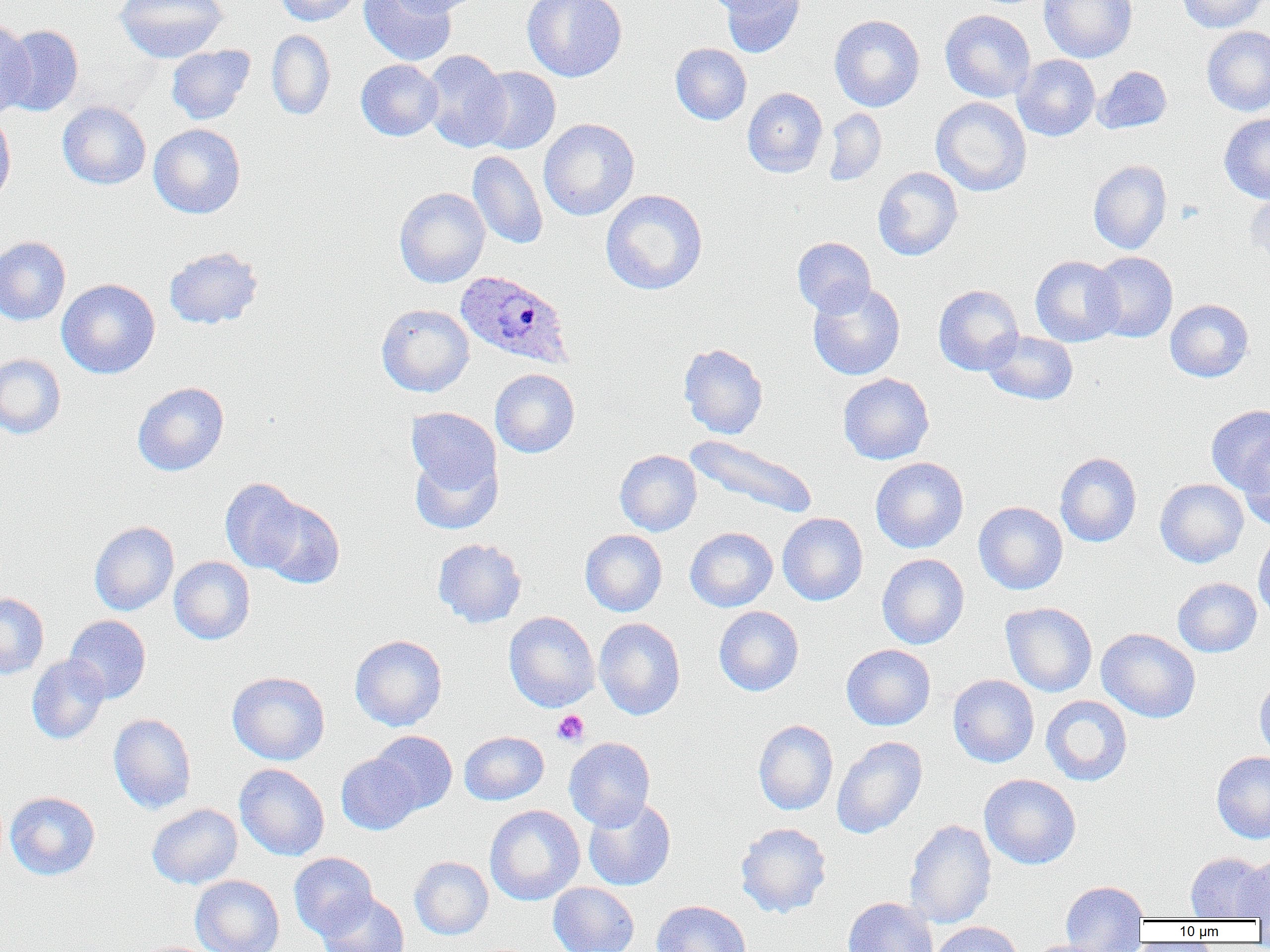

Approximate bounding boxes as [x1, y1, x2, y2] in pixels. Plasmodium ovale-infected red blood cell locations: [455, 269, 574, 369]. Platelet locations: [552, 709, 589, 746]. Uninfected red blood cell locations: [115, 0, 228, 63], [274, 0, 363, 26], [359, 0, 457, 66], [389, 0, 481, 16], [522, 0, 627, 82], [701, 0, 795, 18], [718, 0, 807, 58], [1039, 0, 1137, 63], [1177, 0, 1267, 33], [940, 10, 1036, 102], [829, 14, 925, 112], [0, 17, 35, 119], [1, 24, 83, 117], [1201, 26, 1270, 116], [266, 30, 336, 120], [670, 43, 752, 125], [166, 45, 255, 125], [420, 49, 511, 152], [1013, 55, 1100, 141], [355, 59, 443, 141], [1094, 65, 1172, 134], [473, 67, 560, 154], [742, 87, 828, 178], [931, 97, 1031, 196], [57, 101, 151, 189], [0, 108, 16, 209], [823, 108, 887, 186], [1219, 114, 1270, 203], [538, 118, 639, 221], [149, 123, 246, 218], [467, 150, 548, 249], [1088, 160, 1172, 255], [872, 167, 963, 261], [394, 187, 490, 287], [1246, 187, 1270, 268], [600, 189, 708, 295], [0, 236, 71, 325], [792, 237, 876, 317], [164, 246, 264, 329], [1088, 251, 1178, 342], [1030, 255, 1123, 347], [56, 279, 160, 379], [807, 282, 905, 381], [933, 284, 1024, 375], [1165, 299, 1253, 382], [376, 303, 474, 397], [982, 331, 1079, 405], [678, 343, 768, 439], [0, 353, 66, 439], [490, 368, 580, 457], [838, 373, 934, 464], [132, 382, 229, 476], [1206, 405, 1270, 494], [406, 407, 501, 494], [684, 434, 818, 520], [1238, 438, 1270, 531], [614, 449, 702, 536], [409, 450, 502, 535], [1054, 452, 1142, 547], [870, 457, 969, 553], [220, 477, 306, 573], [1155, 479, 1248, 567], [257, 497, 344, 589], [973, 501, 1068, 594], [777, 513, 867, 605], [89, 521, 179, 615], [685, 527, 777, 612], [580, 530, 667, 616], [1253, 532, 1270, 622], [432, 538, 527, 628], [877, 553, 969, 649], [169, 556, 255, 645], [1172, 577, 1262, 657], [0, 593, 49, 679], [1001, 602, 1097, 696], [714, 606, 804, 696], [504, 611, 600, 712], [64, 615, 151, 704], [594, 618, 685, 720], [1096, 628, 1201, 723], [349, 634, 447, 731], [841, 644, 935, 730], [27, 654, 110, 744], [227, 671, 329, 765], [1254, 673, 1270, 762], [948, 674, 1039, 767], [1041, 695, 1133, 786], [108, 713, 196, 814], [753, 719, 839, 815], [370, 730, 457, 814], [459, 730, 549, 805], [831, 736, 928, 839], [564, 737, 655, 830], [1211, 751, 1270, 843], [336, 753, 422, 835], [235, 764, 329, 861], [979, 774, 1081, 869], [4, 791, 100, 881], [583, 797, 676, 891], [146, 803, 243, 889], [485, 805, 584, 905], [904, 819, 996, 929], [735, 822, 832, 918], [289, 852, 377, 939], [1185, 852, 1268, 920], [1237, 855, 1270, 919], [409, 856, 493, 940], [190, 875, 284, 952], [1060, 880, 1148, 952], [548, 882, 639, 952], [318, 892, 410, 952], [843, 897, 938, 952], [652, 899, 751, 952], [930, 921, 1024, 952], [1025, 939, 1117, 952]. Slide-level diagnosis: Plasmodium ovale. Single field of view. Image is 1270×952 pixels. Optical microscopy. 1000x magnification. Thin blood film.